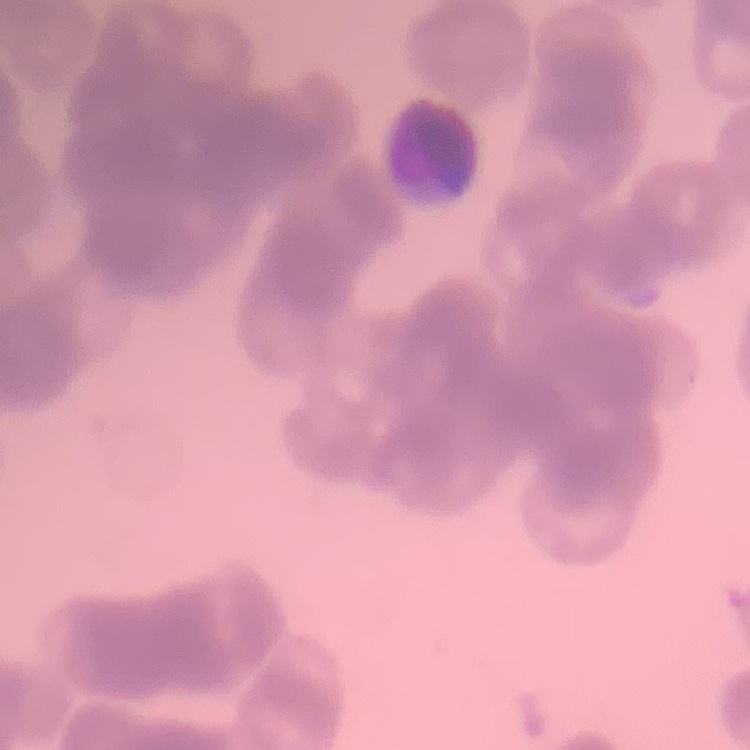
Summary:
  - Erythrocyte morphology: rouleaux formation
  - Preparation: thin blood smear
  - Image type: square crop of a larger photomicrograph
  - Stain: Field's or Giemsa